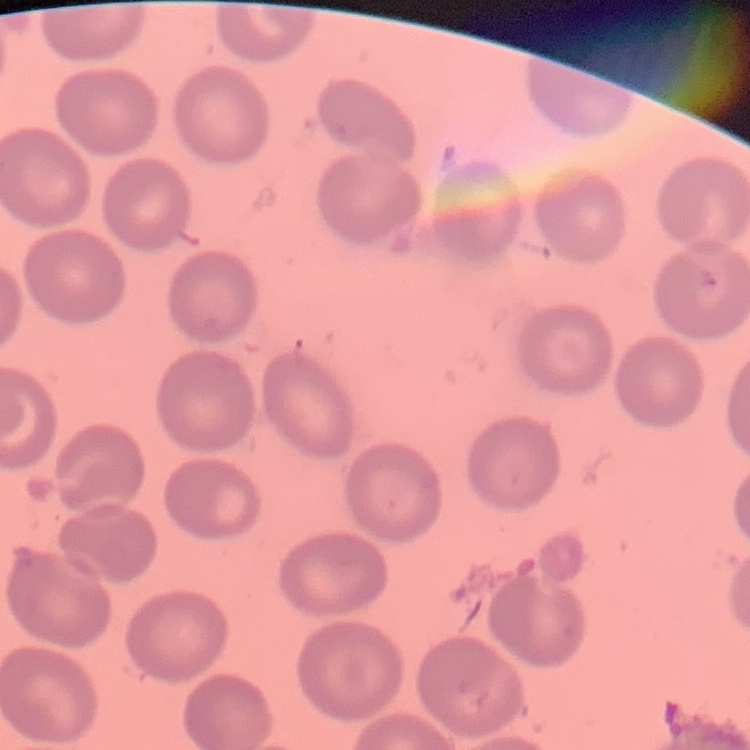

red blood cell morphology = no rouleaux formation
stain = Field's or Giemsa
preparation = thin peripheral smear
image type = one tile cut from a larger photomicrograph